Identify the cell.
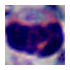

This is a leukocyte.

modality = photomicrograph
magnification = 1000x